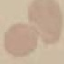 Result: no malaria parasites detected. Thin blood smear. Acquired by smartphone through the microscope eyepiece. Automatically extracted cell patch, resized to 64 × 64 pixels. Giemsa stain.